Give the position of every Plasmodium parasite.
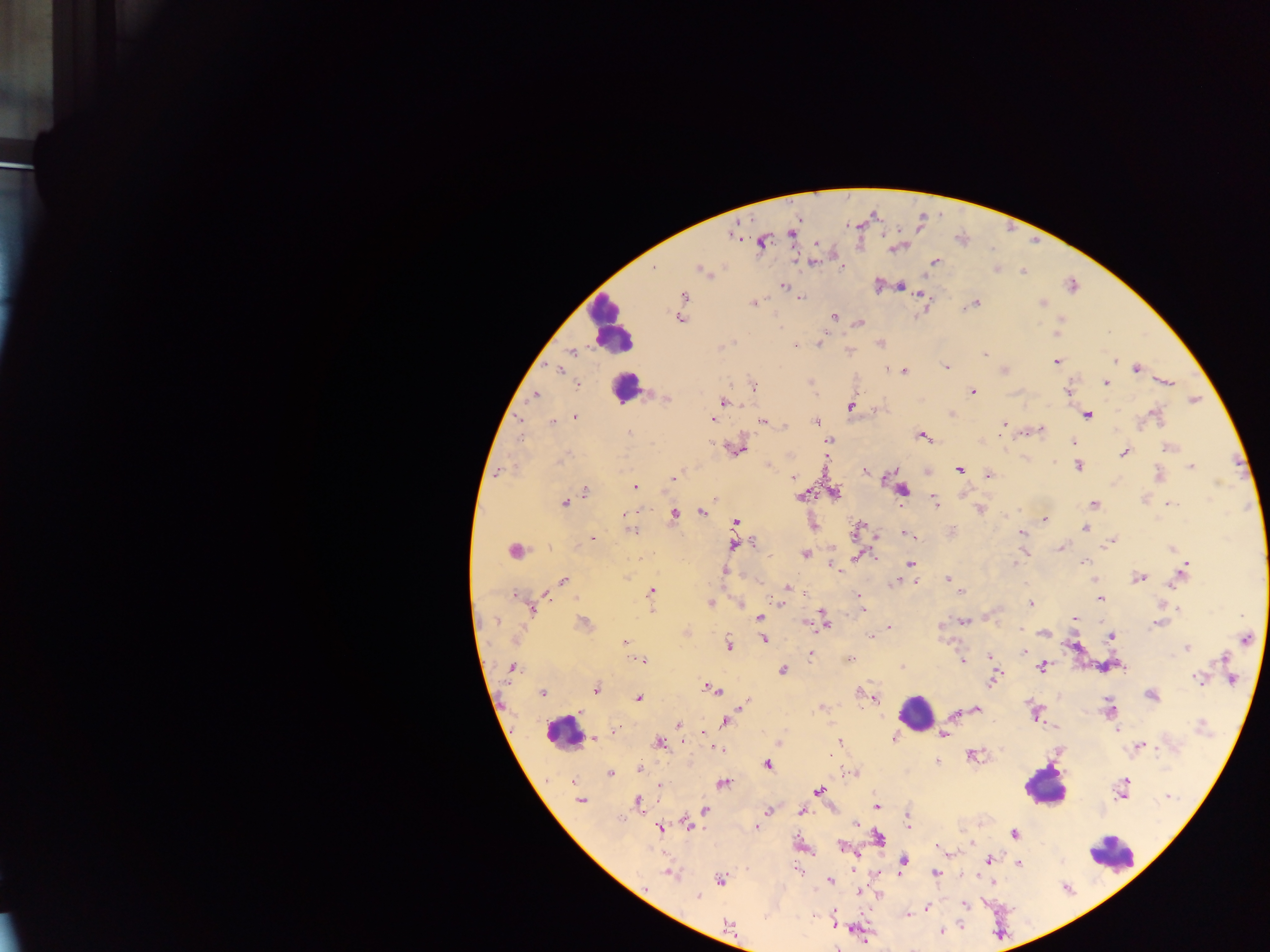
Approximate centers as {x, y} in pixels.
Plasmodium parasites: {792, 234}, {762, 241}, {812, 262}, {934, 262}, {842, 267}, {654, 269}, {996, 269}, {702, 270}, {1023, 271}, {784, 286}, {877, 286}, {901, 286}, {1072, 286}, {684, 296}, {921, 296}, {800, 298}, {753, 303}, {975, 303}, {1042, 303}, {968, 306}, {833, 316}, {680, 319}, {860, 324}, {1057, 333}, {820, 340}, {732, 341}, {796, 347}, {572, 352}, {984, 354}, {1115, 361}, {1056, 362}, {946, 366}, {1136, 368}, {558, 369}, {887, 370}, {1005, 371}, {903, 372}, {811, 382}, {1167, 382}, {1106, 383}, {578, 384}, {753, 387}, {1067, 390}, {973, 392}, {534, 395}, {667, 398}, {1195, 400}, {724, 402}, {851, 405}, {1153, 413}, {952, 414}, {1087, 415}, {575, 416}, {521, 418}, {713, 419}, {762, 421}, {552, 422}, {816, 422}, {1004, 424}, {785, 427}, {1041, 429}, {629, 432}, {922, 436}, {522, 438}, {828, 440}, {1073, 442}, {1169, 447}, {739, 450}, {1124, 452}, {563, 458}, {1053, 463}, {768, 466}, {1078, 466}, {1192, 467}, {959, 470}, {865, 471}, {500, 472}, {988, 476}, {793, 477}, {674, 478}, {886, 478}, {635, 487}, {903, 490}, {585, 492}, {834, 493}, {802, 496}, {935, 502}, {565, 503}, {1094, 504}, {1170, 504}, {980, 510}, {635, 512}, {624, 513}, {702, 513}, {674, 515}, {1045, 521}, {736, 522}, {857, 528}, {1085, 528}, {631, 531}, {952, 531}, {1022, 533}, {907, 535}, {878, 536}, {593, 538}, {752, 543}, {1111, 543}, {735, 544}, {1061, 548}, {1171, 548}, {514, 551}, {804, 554}, {857, 557}, {1084, 562}, {910, 563}, {1015, 563}, {833, 567}, {1184, 570}, {725, 571}, {1139, 578}, {563, 579}, {947, 579}, {915, 582}, {1177, 582}, {897, 583}, {788, 587}, {652, 591}, {960, 592}, {805, 593}, {516, 596}, {859, 596}, {1100, 598}, {710, 603}, {781, 603}, {1031, 604}, {861, 607}, {1178, 608}, {532, 610}, {652, 611}, {759, 617}, {823, 617}, {1075, 618}, {964, 621}, {494, 622}, {804, 623}, {1159, 623}, {583, 624}, {825, 625}, {889, 628}, {1044, 633}, {871, 636}, {1111, 637}, {764, 639}, {1246, 639}, {625, 642}, {729, 645}, {1187, 649}, {1024, 651}, {810, 654}, {989, 656}, {1223, 658}, {850, 659}, {642, 660}, {962, 660}, {1042, 666}, {511, 667}, {903, 667}, {782, 670}, {1198, 678}, {993, 680}, {1232, 680}, {596, 689}, {713, 690}, {543, 693}, {861, 694}, {866, 696}, {873, 696}, {1151, 696}, {638, 698}, {745, 703}, {821, 707}, {976, 709}, {1109, 709}, {1035, 713}, {954, 715}, {725, 721}, {678, 725}, {1202, 726}, {1116, 729}, {615, 733}, {702, 733}, {943, 734}, {594, 738}, {893, 738}, {839, 742}, {659, 743}, {1139, 746}, {718, 749}, {975, 756}, {937, 762}, {768, 763}, {640, 768}, {851, 773}, {610, 774}, {572, 781}, {724, 784}, {1122, 784}, {660, 785}, {819, 791}, {1169, 796}, {580, 800}, {637, 802}, {876, 806}, {705, 810}, {768, 811}, {801, 811}, {907, 823}, {687, 824}, {856, 824}, {660, 827}, {756, 827}, {1014, 834}, {879, 838}, {843, 848}, {941, 848}, {990, 859}, {904, 861}, {1019, 864}, {669, 873}, {936, 873}, {720, 880}, {830, 881}, {861, 893}, {877, 895}, {698, 896}, {965, 904}, {926, 908}, {923, 910}, {907, 915}, {727, 923}, {835, 923}, {941, 931}.

Summary:
  - Leukocyte locations: {611, 324}, {624, 388}, {916, 712}, {563, 732}, {1044, 787}, {1113, 855}
  - Preparation: thick blood film
  - Country: Ghana
  - Field of view: single
  - Image size: 1270×952 pixels
  - Capture: mobile-phone photograph through a microscope